Comment on the morphology of the red blood cells.
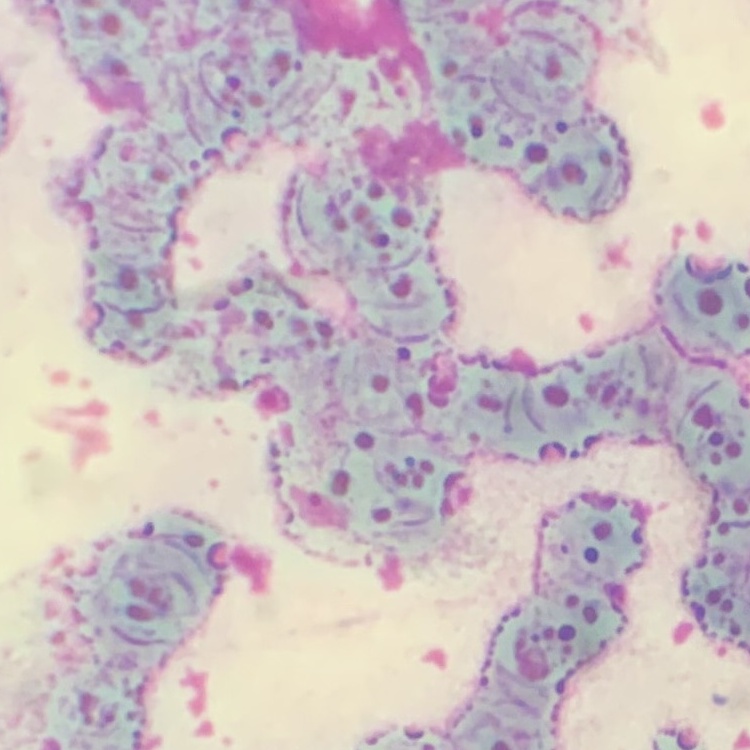
They show rouleaux formation.

image_type: one tile cut from a larger photomicrograph
stain: Field's or Giemsa
preparation: thin blood smear